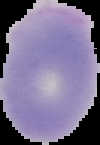

From a thin blood film. Result: no Plasmodium parasites seen. Image is 100×145 pixels. Cell region segmented out of the field of view; the surrounding area is masked to black.